Name the parasite shown.
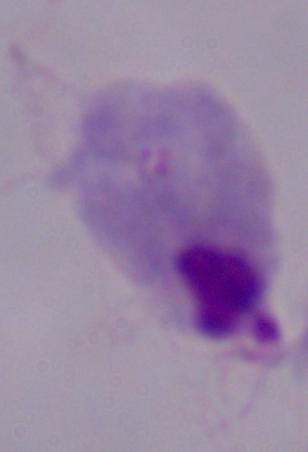

A trichomonad.

Summary:
  - Modality: photomicrograph
  - Magnification: 1000x